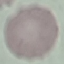
malaria_status: uninfected
capture: smartphone through the microscope eyepiece
preparation: thin smear
image_type: automatically extracted cell patch, resized to 64 × 64 pixels
stain: Giemsa